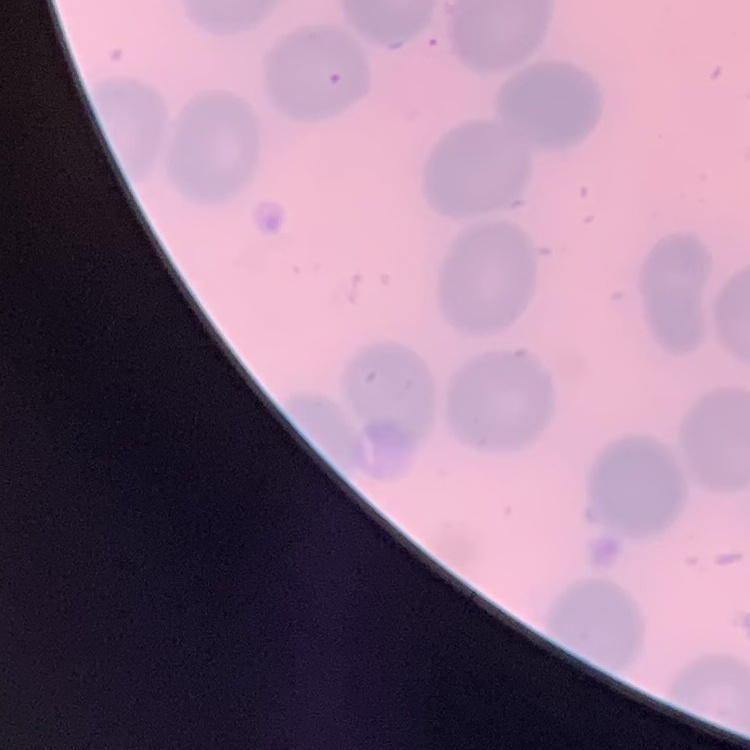
Summary:
  - Red blood cell morphology: no rouleaux formation
  - Preparation: thin blood smear
  - Stain: Field's or Giemsa
  - Image type: one tile cut from a larger photomicrograph